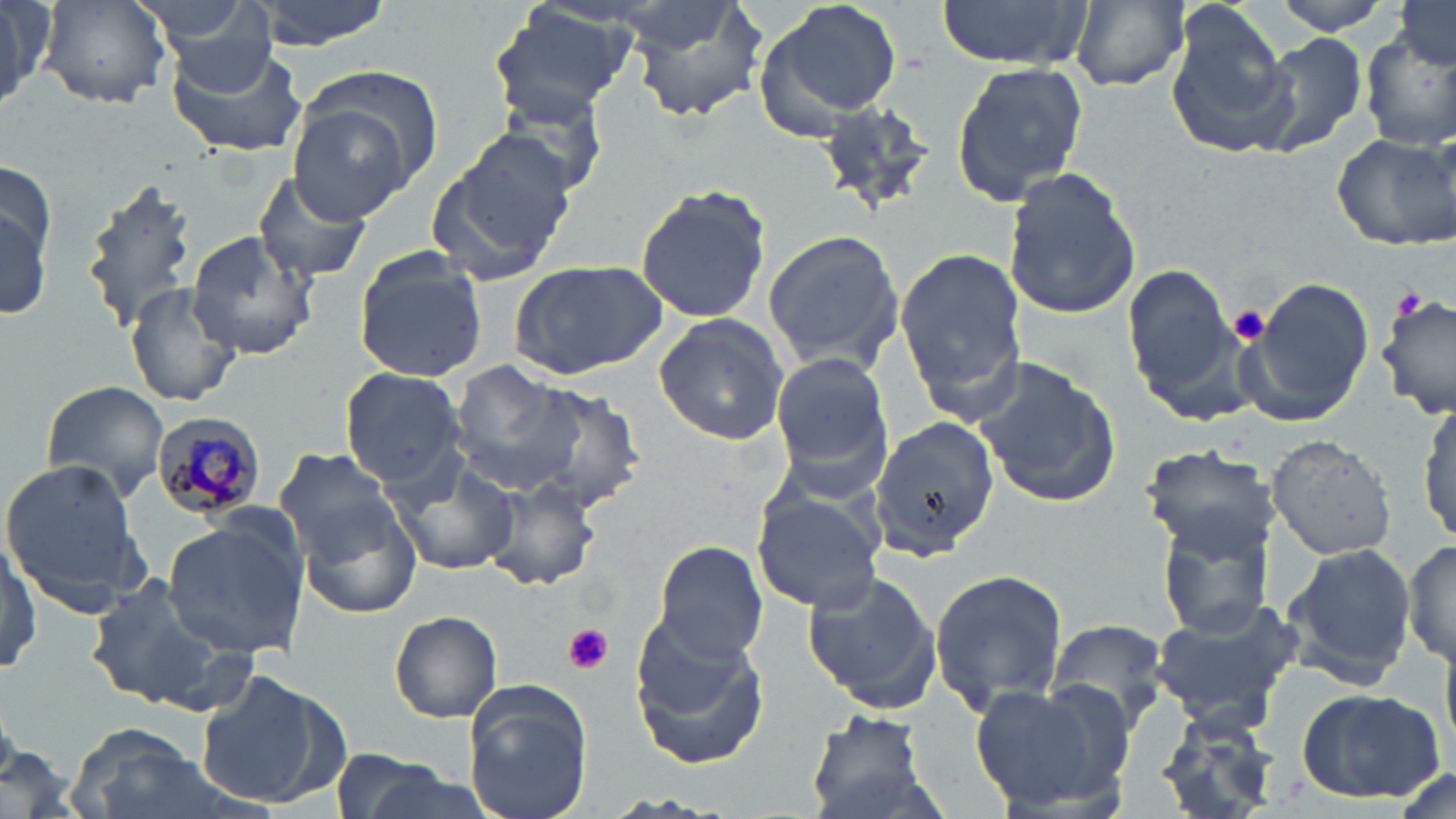 Approximate bounding boxes as (x1,y1)-(x2,y2) corner pairs in pixels. Plasmodium malariae-infected red blood cell locations: (151,412)-(266,520). Uninfected red blood cell locations: (0,0)-(56,110), (37,0)-(174,110), (249,0)-(394,53), (622,0)-(769,125), (754,0)-(905,138), (935,0)-(1094,70), (1268,0)-(1403,35), (152,1)-(289,86), (1391,1)-(1456,71), (1066,2)-(1190,92), (487,4)-(641,123), (942,6)-(1082,144), (1164,6)-(1296,162), (1250,28)-(1371,160), (1359,33)-(1456,153), (165,41)-(307,160), (951,58)-(1090,208), (299,66)-(442,189), (483,85)-(614,202), (813,98)-(940,222), (287,101)-(418,223), (1330,131)-(1456,249), (426,132)-(577,287), (1000,165)-(1141,322), (250,171)-(374,285), (79,177)-(199,334), (634,182)-(772,324), (0,197)-(51,319), (762,226)-(906,376), (186,231)-(319,361), (891,241)-(1027,427), (354,251)-(487,383), (509,259)-(669,383), (1123,261)-(1243,409), (1244,276)-(1373,423), (123,282)-(242,407), (1378,293)-(1456,422), (653,314)-(791,446), (770,355)-(893,478), (973,356)-(1122,511), (452,361)-(585,496), (340,366)-(467,489), (39,379)-(169,507), (522,385)-(647,513), (1417,395)-(1455,547), (868,413)-(999,561), (1264,432)-(1401,560), (1139,443)-(1279,559), (273,444)-(404,571), (385,450)-(520,579), (0,456)-(151,617), (478,475)-(599,592), (753,492)-(884,612), (297,495)-(424,619), (1152,509)-(1281,632), (163,518)-(309,660), (0,529)-(40,684), (1403,538)-(1456,668), (1280,539)-(1418,688), (652,540)-(768,665), (928,566)-(1067,717), (803,567)-(942,713), (85,574)-(252,717), (1144,600)-(1306,732), (388,610)-(503,723), (628,617)-(771,767), (1048,617)-(1172,727), (197,668)-(348,808), (968,680)-(1133,816), (463,681)-(593,819), (1295,686)-(1447,806), (806,710)-(933,817), (1155,714)-(1285,818), (66,723)-(215,819), (327,751)-(468,819). Platelet locations: (1391,286)-(1426,320), (1227,306)-(1272,346), (562,623)-(612,676). Slide-level diagnosis: Plasmodium malariae. Light microscopy. Thin blood film. Image is 1456×819 pixels. Single field of view. 1000x magnification. May-Grünwald-Giemsa-stained preparation.